Assess this cell for malaria.
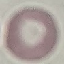
It is uninfected.

Summary:
  - Preparation: thin blood film
  - Image type: cell patch, automatically extracted from a larger field of view and resized to 64 × 64 pixels
  - Capture: smartphone camera at the microscope eyepiece
  - Stain: Giemsa